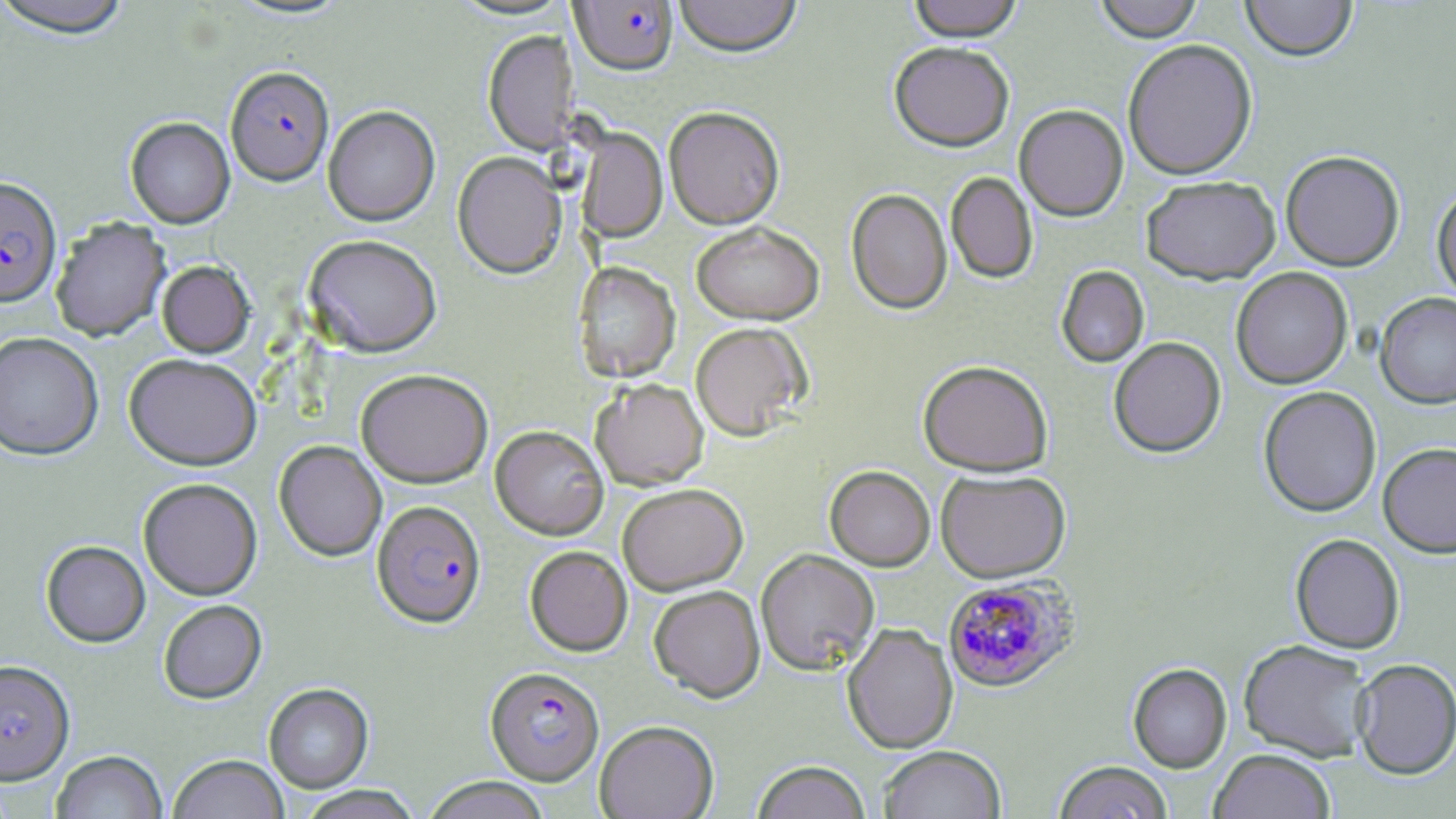
Summary:
  - Coordinate format: approximate bounding boxes as [x1, y1, x2, y2] in pixels
  - Plasmodium falciparum-infected red blood cell locations: [569, 1, 679, 76], [225, 66, 334, 185], [0, 177, 62, 307], [372, 500, 486, 628], [945, 576, 1084, 693], [0, 660, 74, 784], [485, 666, 604, 785]
  - Uninfected red blood cell locations: [0, 0, 136, 38], [673, 0, 802, 58], [907, 0, 1023, 41], [1093, 0, 1204, 43], [1240, 0, 1358, 62], [483, 29, 577, 155], [1122, 38, 1258, 180], [889, 42, 1014, 151], [1014, 104, 1128, 221], [323, 105, 440, 225], [663, 106, 785, 229], [125, 117, 235, 228], [577, 129, 668, 241], [1281, 150, 1405, 271], [452, 152, 565, 278], [946, 172, 1038, 284], [1141, 176, 1280, 284], [1432, 185, 1456, 305], [846, 188, 952, 314], [50, 217, 170, 341], [691, 221, 825, 325], [303, 234, 442, 357], [157, 261, 254, 358], [573, 261, 681, 382], [1056, 265, 1149, 368], [1231, 268, 1352, 389], [1375, 292, 1456, 409], [689, 322, 811, 440], [0, 332, 104, 460], [1109, 336, 1226, 458], [124, 353, 262, 470], [917, 359, 1053, 477], [355, 368, 493, 487], [591, 377, 709, 490], [1258, 386, 1382, 517], [490, 425, 608, 539], [274, 440, 387, 561], [1378, 443, 1456, 557], [825, 465, 935, 571], [936, 469, 1070, 583], [138, 478, 262, 599], [617, 483, 748, 594], [1290, 533, 1405, 653], [41, 540, 150, 647], [525, 546, 632, 656], [755, 549, 879, 675], [649, 585, 765, 702], [158, 600, 267, 704], [842, 623, 958, 753], [1238, 639, 1373, 762], [1352, 659, 1456, 779], [1127, 663, 1232, 773], [263, 683, 374, 793], [595, 720, 718, 819], [877, 745, 1006, 819], [1209, 748, 1335, 819], [51, 750, 167, 819], [168, 754, 288, 819], [752, 760, 871, 819], [1054, 761, 1172, 819], [422, 777, 551, 819], [295, 786, 422, 819]
  - Slide-level diagnosis: Plasmodium falciparum
  - Preparation: thin blood smear
  - Modality: optical microscopy
  - Magnification: 1000x
  - Field of view: single
  - Image size: 1456×819 pixels
  - Stain: May-Grünwald-Giemsa